State the blood parasite species.
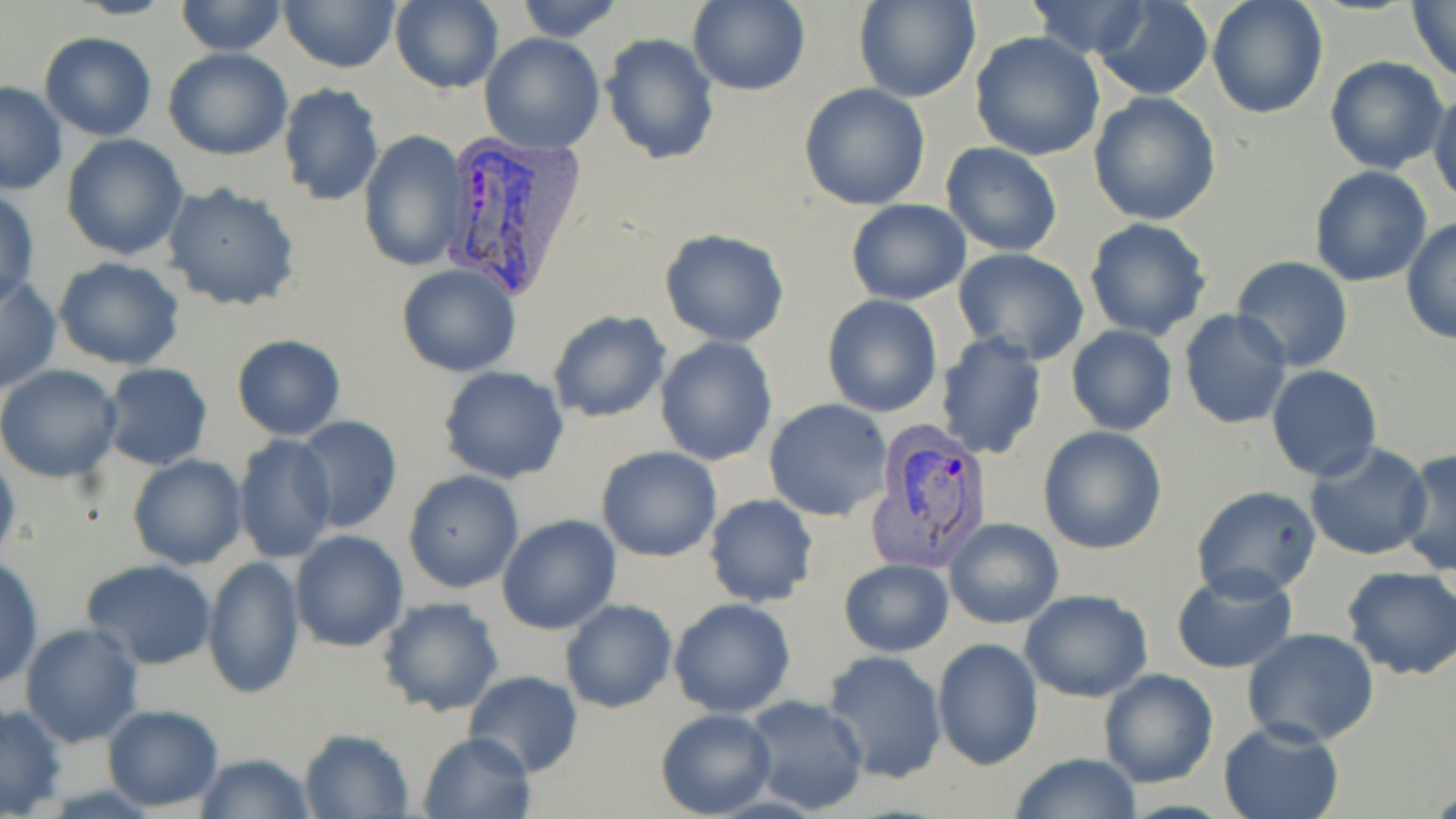
Plasmodium vivax.

Approximate bounding boxes as (x1,y1)-(x2,y2) corner pairs in pixels. Uninfected red blood cell locations: (174,0)-(291,55), (279,0)-(400,73), (390,0)-(504,95), (513,0)-(624,41), (856,0)-(980,103), (1091,0)-(1214,100), (1207,0)-(1328,119), (1406,0)-(1456,82), (687,1)-(810,95), (1023,2)-(1153,59), (969,31)-(1105,161), (38,32)-(157,141), (478,33)-(605,154), (601,33)-(720,165), (163,49)-(294,161), (1323,54)-(1449,173), (0,82)-(68,195), (278,82)-(385,207), (799,82)-(931,211), (1429,89)-(1456,206), (1088,91)-(1221,226), (358,130)-(469,271), (62,134)-(189,260), (940,142)-(1065,256), (1308,165)-(1433,287), (161,182)-(301,313), (0,190)-(39,308), (845,199)-(971,306), (1084,217)-(1211,341), (1400,217)-(1456,346), (659,229)-(790,346), (952,250)-(1090,365), (1232,255)-(1354,372), (52,258)-(187,369), (395,262)-(521,377), (0,276)-(60,393), (822,294)-(943,419), (547,309)-(670,424), (1178,309)-(1293,430), (1065,325)-(1177,435), (935,332)-(1048,460), (230,335)-(346,439), (654,336)-(778,466), (101,363)-(214,470), (0,364)-(124,483), (439,366)-(570,483), (1265,366)-(1382,482), (764,399)-(892,521), (292,416)-(405,534), (1037,426)-(1167,555), (233,434)-(338,562), (1303,443)-(1434,561), (1397,446)-(1456,576), (596,447)-(721,562), (0,448)-(19,566), (127,455)-(247,570), (403,471)-(523,593), (1192,486)-(1324,602), (704,493)-(818,608), (496,515)-(622,634), (945,518)-(1063,629), (289,529)-(409,653), (1,557)-(43,687), (202,557)-(305,699), (82,559)-(217,670), (148,559)-(275,682), (839,559)-(954,657), (1170,565)-(1298,675), (1342,566)-(1456,680), (1020,589)-(1153,702), (376,596)-(505,717), (668,598)-(797,718), (559,600)-(677,714), (1041,608)-(1180,748), (19,623)-(144,747), (1241,629)-(1382,748), (932,638)-(1043,771), (820,649)-(946,782), (1098,668)-(1217,788), (464,671)-(582,778), (737,695)-(871,815), (1,703)-(68,817), (104,704)-(224,813), (654,708)-(776,817), (1217,719)-(1346,819), (298,728)-(415,818), (417,729)-(534,819), (1011,752)-(1142,819), (194,754)-(315,819). Plasmodium vivax-infected red blood cell locations: (438,133)-(582,299), (869,422)-(996,570). 1000x magnification. One field of a larger specimen. May-Grünwald-Giemsa stain. Thin blood smear. Image is 1456×819 pixels. Light microscopy.